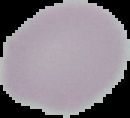
From a thin blood film. Malaria status: uninfected. Image is 130×118 pixels. Segmented cell region on a black background.